Locate every blood parasite and identify its species.
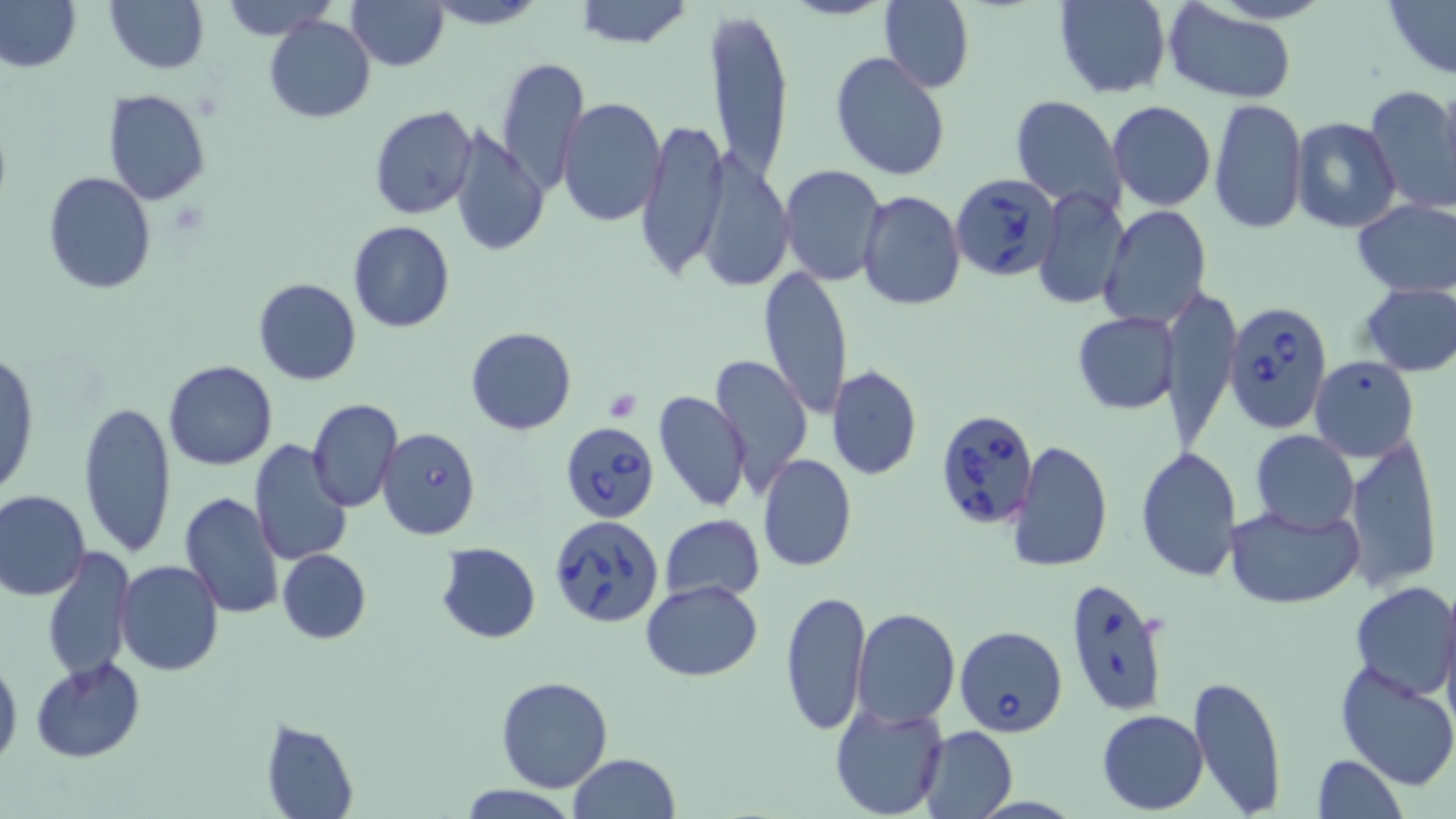

Approximate bounding boxes as (x1, y1, x2, y2) in pixels.
Babesia divergens-infected red blood cells: (951, 172, 1063, 282), (1223, 298, 1333, 436), (935, 407, 1042, 530), (558, 420, 659, 523), (376, 427, 481, 540), (550, 514, 664, 629), (1064, 578, 1171, 717), (954, 624, 1068, 738).
No Plasmodium falciparum, Plasmodium ovale, Plasmodium malariae, Plasmodium vivax, or Trypanosoma brucei observed.

Summary:
  - Uninfected red blood cell locations: (216, 0, 342, 39), (346, 0, 448, 70), (422, 0, 548, 29), (1382, 0, 1455, 78), (1, 1, 80, 73), (105, 1, 208, 74), (573, 1, 693, 49), (878, 1, 974, 90), (1054, 1, 1172, 99), (1162, 3, 1298, 104), (704, 10, 789, 183), (265, 16, 375, 123), (830, 52, 951, 181), (495, 56, 588, 194), (1366, 85, 1456, 213), (103, 89, 212, 205), (1009, 95, 1126, 211), (556, 97, 666, 226), (1209, 98, 1306, 235), (1107, 101, 1216, 212), (369, 105, 477, 219), (1289, 116, 1401, 233), (635, 118, 728, 283), (447, 124, 549, 260), (705, 156, 798, 287), (777, 164, 887, 286), (43, 172, 157, 295), (1032, 185, 1130, 312), (860, 190, 966, 310), (1353, 197, 1456, 298), (1101, 206, 1212, 331), (349, 221, 454, 333), (761, 265, 853, 420), (253, 278, 361, 385), (1358, 281, 1455, 376), (1163, 283, 1242, 449), (1072, 311, 1178, 414), (465, 325, 576, 434), (1, 347, 38, 498), (709, 355, 814, 493), (1308, 357, 1419, 460), (164, 360, 277, 469), (826, 365, 923, 481), (652, 389, 750, 512), (306, 398, 403, 512), (78, 399, 176, 559), (1250, 430, 1360, 534), (1344, 433, 1441, 591), (1009, 438, 1113, 576), (248, 440, 353, 570), (1136, 448, 1242, 583), (758, 453, 857, 571), (0, 489, 91, 600), (178, 491, 285, 621), (1224, 502, 1363, 609), (660, 513, 765, 600), (435, 542, 542, 642), (42, 546, 134, 683), (277, 549, 370, 644), (114, 559, 225, 675), (642, 581, 763, 681), (1350, 582, 1456, 702), (1436, 582, 1456, 717), (779, 588, 872, 735), (850, 609, 961, 728), (0, 654, 22, 773), (30, 656, 144, 763), (1334, 659, 1456, 790), (1187, 673, 1287, 817), (496, 674, 614, 791), (829, 702, 948, 819), (1096, 709, 1208, 814), (260, 718, 359, 819), (916, 726, 1018, 817), (569, 753, 680, 819), (1311, 754, 1407, 819), (457, 784, 578, 818)
  - Platelet locations: (605, 388, 641, 421)
  - Slide-level diagnosis: Babesia divergens
  - Stain: May-Grünwald-Giemsa
  - Modality: optical microscopy
  - Magnification: 1000x
  - Image size: 1456×819 pixels
  - Preparation: thin blood film
  - Field of view: one of a larger specimen